Identify the parasite.
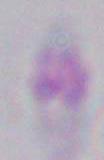

Toxoplasma gondii.

Summary:
  - Modality: micrograph
  - Magnification: 1000x